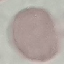
Summary:
  - Result: negative for malaria parasites
  - Image type: cell patch, automatically extracted from a larger field of view and resized to 64 × 64 pixels
  - Stain: Giemsa
  - Capture: smartphone camera at the microscope eyepiece
  - Preparation: thin blood film